Comment on the morphology of the erythrocytes.
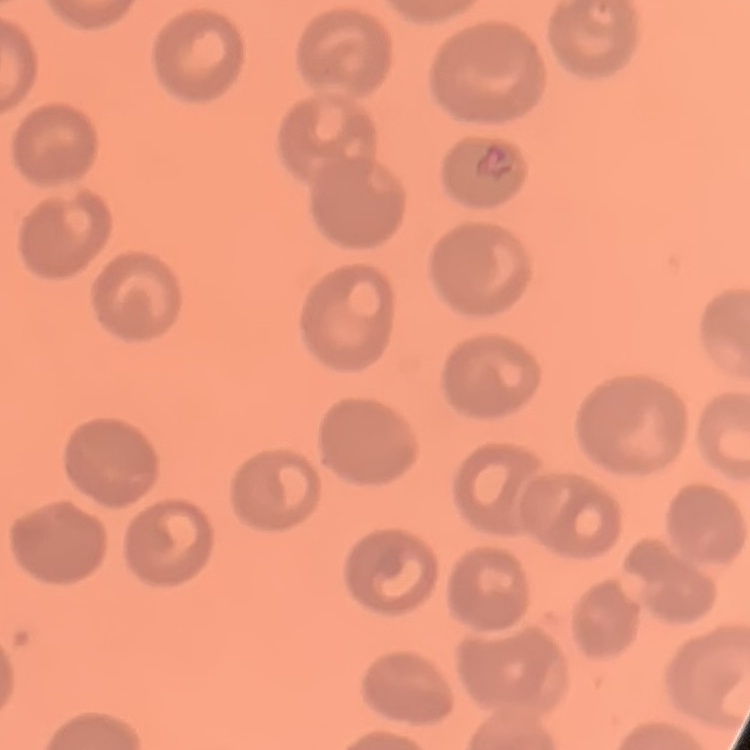
They show no rouleaux formation.

One tile cut from a larger photomicrograph. Field's or Giemsa stain. Thin blood film.